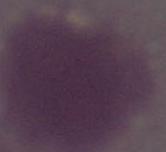

magnification: 1000x
identification: red blood cell
modality: photomicrograph